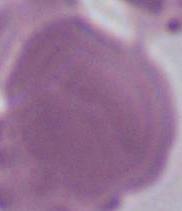

Summary:
  - Modality: micrograph
  - Magnification: 1000x
  - Identification: erythrocyte